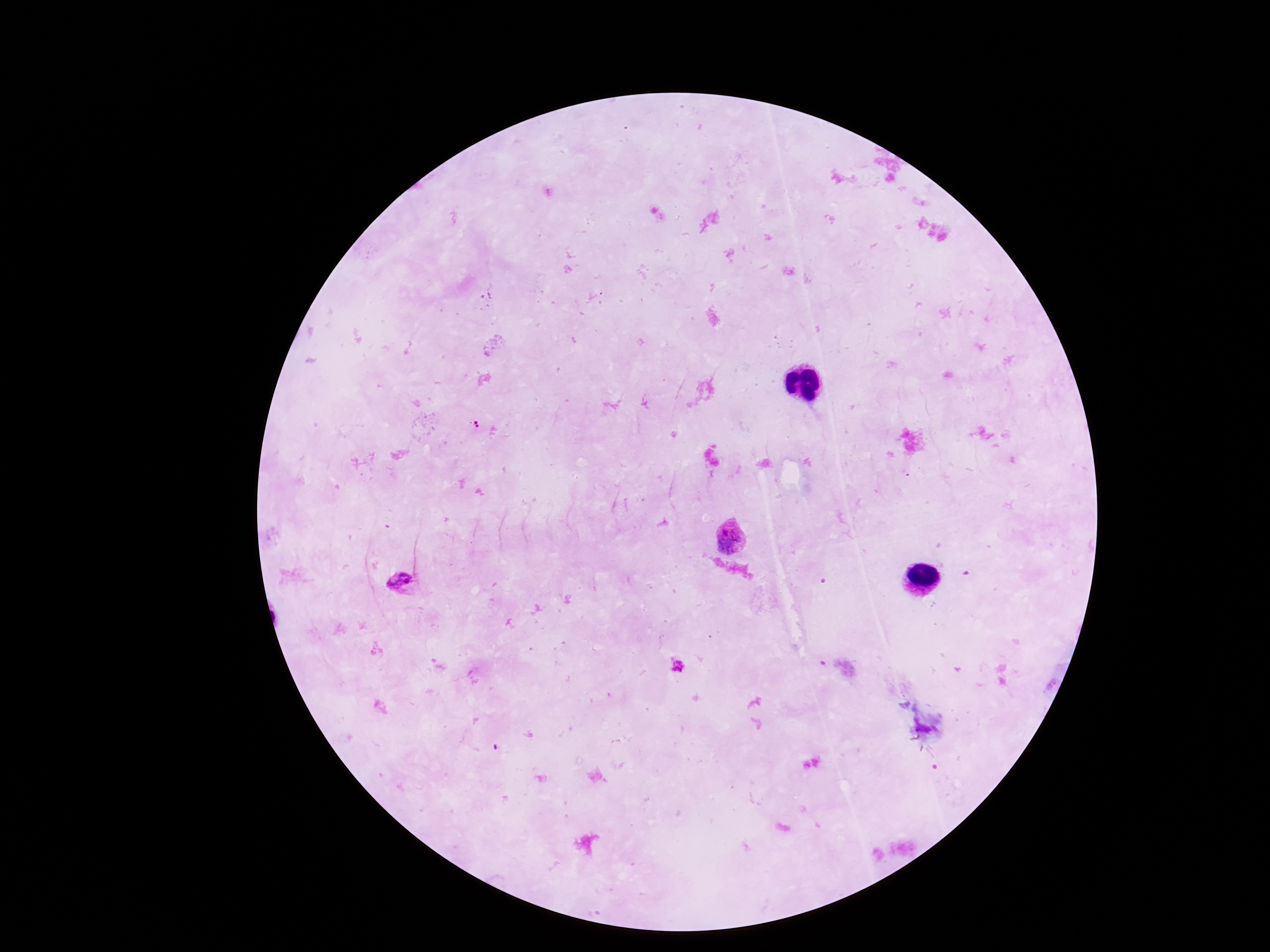
Plasmodium parasite locations = approximate object centers, in pixels from the top-left corner: (x=476, y=427), (x=731, y=538), (x=406, y=581), (x=677, y=668)
capture = smartphone camera through the microscope eyepiece
patient malaria status = positive
field of view = single
preparation = thick blood film
image size = 1270×952 pixels
stain = Giemsa
magnification = 100x